Outline each Plasmodium vivax-infected red blood cell.
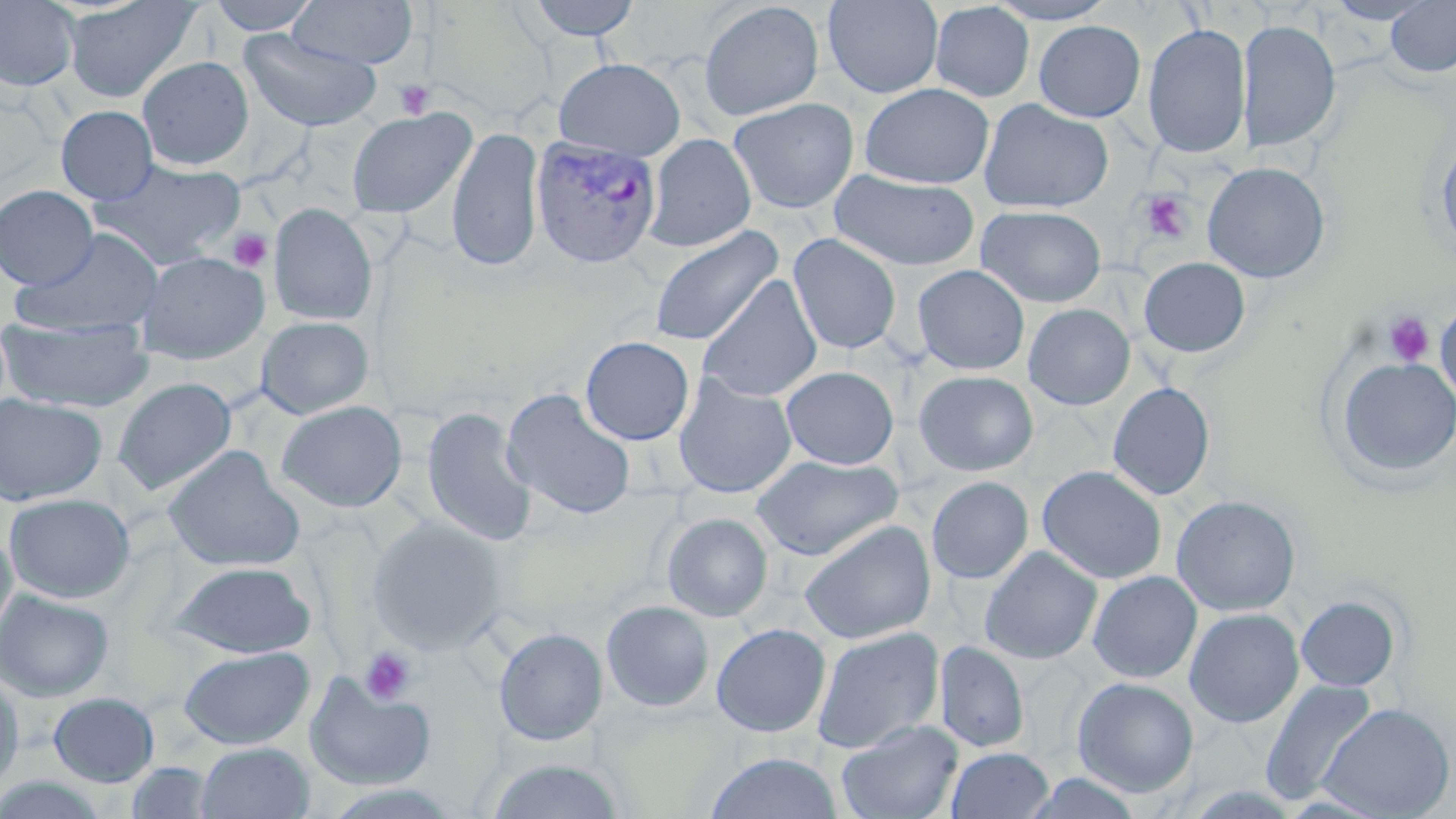

Approximate bounding boxes as (x1,y1)-(x2,y2) corner pairs in pixels.
Plasmodium vivax-infected red blood cells: (532,134)-(662,268).

Uninfected red blood cell locations: (62,0)-(202,103), (206,0)-(324,35), (523,0)-(642,40), (822,0)-(943,98), (984,0)-(1119,24), (1323,0)-(1438,25), (0,1)-(80,91), (290,1)-(418,69), (419,1)-(557,123), (699,1)-(824,120), (1385,1)-(1456,79), (929,2)-(1035,102), (1033,19)-(1145,122), (1237,19)-(1341,153), (1142,23)-(1251,159), (239,29)-(382,132), (138,56)-(254,170), (554,57)-(686,160), (859,83)-(994,189), (728,97)-(859,214), (979,98)-(1114,214), (56,105)-(158,205), (347,107)-(475,219), (447,125)-(545,272), (644,134)-(756,252), (1436,136)-(1456,258), (94,159)-(246,268), (1203,162)-(1331,283), (831,169)-(979,271), (0,185)-(99,290), (268,203)-(377,325), (975,205)-(1106,308), (648,225)-(783,347), (12,228)-(165,337), (788,233)-(902,354), (136,251)-(269,364), (1139,257)-(1251,358), (912,264)-(1030,375), (698,274)-(822,402), (1435,301)-(1456,405), (1023,303)-(1135,410), (0,315)-(154,412), (256,315)-(374,419), (580,336)-(694,445), (1335,357)-(1456,479), (781,366)-(898,469), (913,370)-(1038,476), (673,374)-(797,499), (113,377)-(237,496), (1107,382)-(1215,501), (501,388)-(637,520), (0,394)-(108,506), (277,401)-(408,512), (421,406)-(538,547), (163,445)-(305,573), (751,455)-(902,560), (1037,465)-(1167,584), (927,476)-(1033,584), (4,493)-(135,603), (1171,495)-(1301,616), (662,513)-(772,622), (367,517)-(506,655), (799,520)-(936,644), (0,525)-(18,649), (980,546)-(1102,664), (168,561)-(316,658), (1087,571)-(1202,683), (0,588)-(114,702), (1296,595)-(1401,691), (601,600)-(715,712), (1184,608)-(1304,728), (711,623)-(830,737), (812,626)-(944,753), (494,627)-(608,745), (934,641)-(1029,753), (178,645)-(315,749), (0,669)-(26,795), (304,673)-(436,790), (1072,677)-(1199,797), (1260,678)-(1377,807), (48,692)-(160,787), (1317,702)-(1454,818), (836,719)-(963,819), (195,741)-(315,819), (947,748)-(1054,819), (704,751)-(844,819), (485,758)-(627,818), (125,761)-(216,818), (0,772)-(115,818). Platelet locations: (394,79)-(436,119), (1135,190)-(1194,245), (227,228)-(272,273), (1383,311)-(1435,367), (360,646)-(418,704). Slide-level diagnosis: Plasmodium vivax. May-Grünwald-Giemsa stain. Captured at 1000x magnification. Thin blood film. Image is 1456×819 pixels. Optical microscopy. Single field of view.